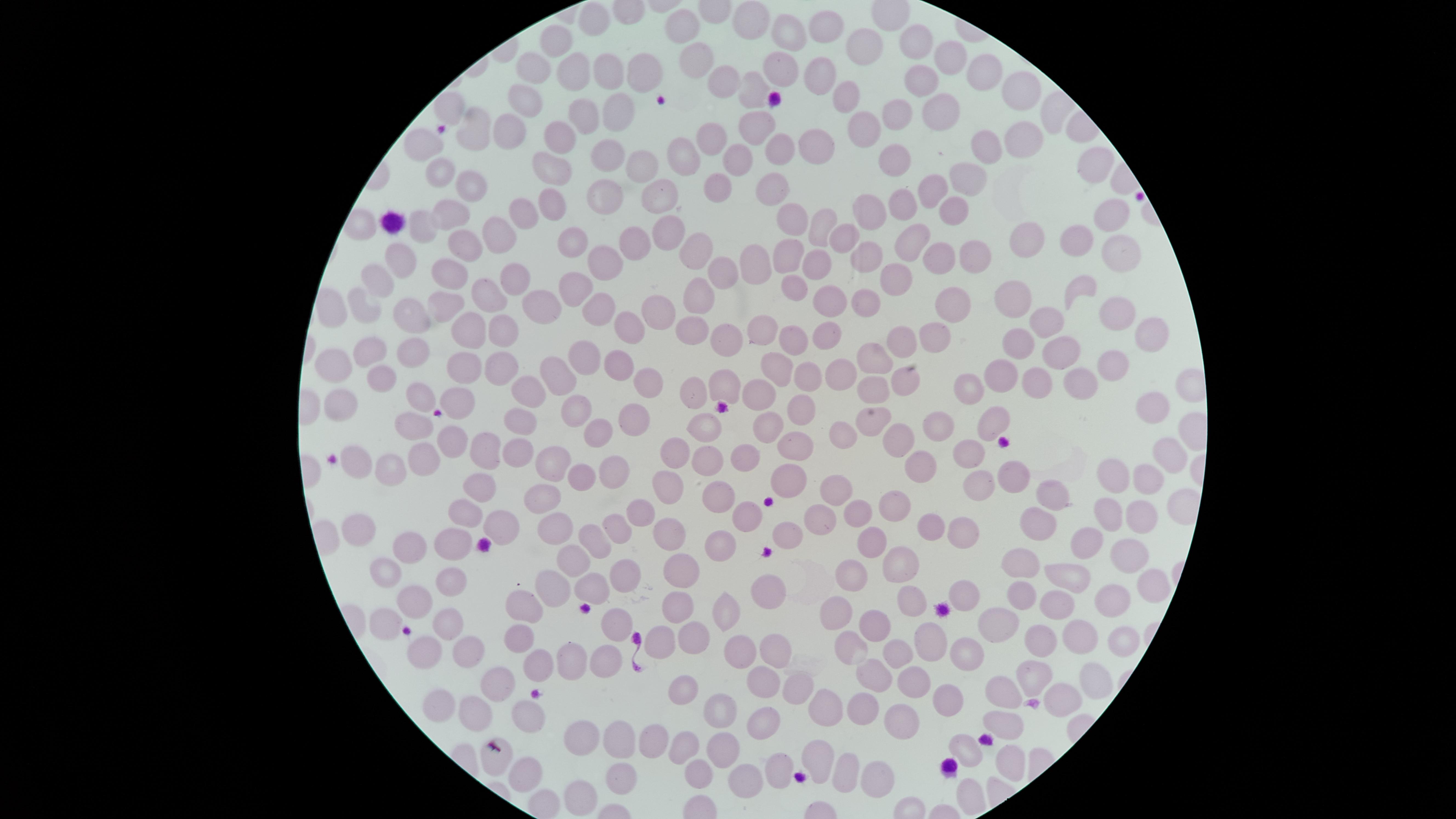

Approximate marker points as [x, y] in pixels. Uninfected red blood cells: [752, 15], [597, 25], [688, 27], [832, 28], [793, 33], [925, 36], [556, 40], [865, 44], [956, 54], [701, 61], [779, 68], [608, 69], [533, 70], [985, 72], [576, 73], [645, 73], [723, 78], [820, 78], [919, 81], [1022, 83], [750, 88], [520, 94], [842, 99], [936, 101], [454, 104], [896, 109], [614, 111], [579, 117], [760, 122], [478, 125], [515, 126], [859, 131], [557, 134], [707, 137], [426, 138], [815, 142], [781, 144], [983, 144], [1025, 145], [607, 149], [683, 155], [743, 157], [898, 160], [640, 163], [1096, 164], [550, 169], [973, 173], [443, 174], [937, 181], [476, 184], [716, 184], [770, 188], [658, 195], [606, 200], [900, 203], [452, 205], [554, 205], [951, 206], [519, 209], [794, 213], [1104, 213], [862, 214], [824, 225], [498, 226], [671, 226], [420, 228], [1019, 232], [839, 235], [1077, 236], [469, 237], [912, 238], [640, 239], [573, 241], [699, 249], [1118, 251], [787, 252], [402, 253], [936, 253], [762, 255], [862, 257], [979, 258], [600, 261], [819, 263], [727, 264], [456, 269], [517, 273], [902, 276], [379, 277], [793, 286], [1080, 286], [571, 288], [495, 293], [705, 295], [1021, 296], [824, 298], [862, 299], [364, 302], [954, 303], [441, 304], [540, 307], [594, 309], [651, 310], [1112, 310], [407, 312], [1048, 314], [510, 324], [623, 325], [761, 326], [695, 327], [466, 328], [832, 331], [931, 333], [1150, 333], [727, 335], [793, 335], [1060, 344], [897, 345], [1022, 346], [381, 347], [876, 353], [579, 354], [417, 355], [332, 359], [1107, 360], [496, 361], [616, 363], [773, 363], [462, 367], [554, 372], [801, 373], [838, 373], [1004, 373], [381, 374], [1077, 374], [640, 376], [698, 379], [901, 379], [977, 379], [1041, 383], [876, 385], [723, 387], [760, 389], [524, 390], [419, 393], [464, 398], [804, 400], [337, 401], [574, 408], [1154, 410], [520, 417], [629, 417], [939, 418], [766, 420], [992, 421], [707, 422], [411, 423], [890, 432], [595, 433], [843, 433], [452, 442], [793, 444], [489, 448], [672, 448], [967, 448], [517, 452], [920, 453], [1163, 454], [747, 455], [423, 458], [704, 463], [353, 464], [547, 466], [386, 469], [614, 469], [586, 474], [785, 476], [981, 477], [1023, 477], [1153, 479], [1127, 480], [479, 483], [665, 491], [841, 494], [717, 496], [533, 501], [1059, 501], [895, 504], [640, 508], [1106, 508], [862, 509], [465, 510], [1139, 510], [746, 514], [820, 515], [1036, 519], [499, 520], [555, 525], [785, 525], [931, 525], [615, 526], [964, 526], [359, 527], [668, 533], [717, 539], [451, 540], [1096, 540], [871, 541], [594, 542], [406, 548], [1121, 550], [1014, 556], [894, 559], [572, 561], [685, 571], [1070, 572], [381, 574], [852, 574], [625, 575], [1143, 582], [446, 584], [769, 586], [542, 587], [968, 588], [589, 590], [1020, 591], [1108, 593], [411, 596], [907, 599], [1060, 604], [516, 609], [683, 610], [728, 610], [833, 617], [877, 619], [1000, 620], [619, 623], [381, 624], [457, 625], [1044, 630], [693, 632], [931, 633], [1074, 635], [513, 638], [662, 638], [1119, 641], [849, 644], [739, 647], [419, 648], [953, 648], [770, 650], [895, 651], [476, 655], [606, 655], [537, 664], [568, 665], [1032, 673], [870, 676], [761, 682], [499, 684], [917, 684], [1094, 686], [793, 690], [433, 691], [1009, 692], [681, 695], [1061, 698], [948, 700], [722, 704], [863, 704], [481, 705], [826, 709], [529, 717], [1007, 719], [762, 721], [896, 722], [649, 736], [617, 737], [723, 739], [586, 741], [686, 745], [963, 746], [820, 749], [1009, 757], [495, 758], [777, 762], [838, 767], [693, 768], [525, 770], [618, 774], [872, 775], [741, 779], [570, 793]. Thin blood smear. Presence: no malaria parasites identified. Single field of view. Giemsa stain. Image is 1456×819 pixels. Smartphone photograph through the microscope eyepiece. The visible region is circular.